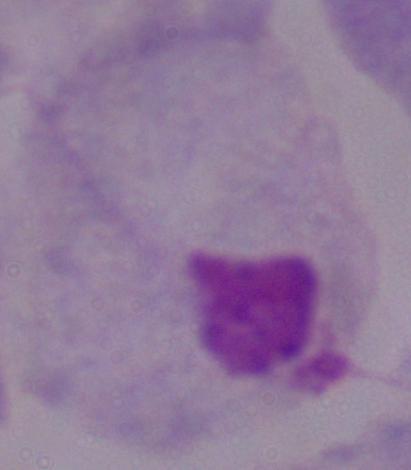

Summary:
  - Magnification: 1000x
  - Identification: trichomonad
  - Modality: micrograph